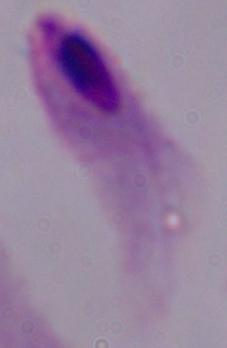
Summary:
  - Magnification: 1000x
  - Identification: trichomonad
  - Modality: photomicrograph